Identify the cell.
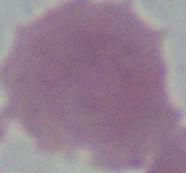
This is an erythrocyte.

modality = micrograph
magnification = 1000x